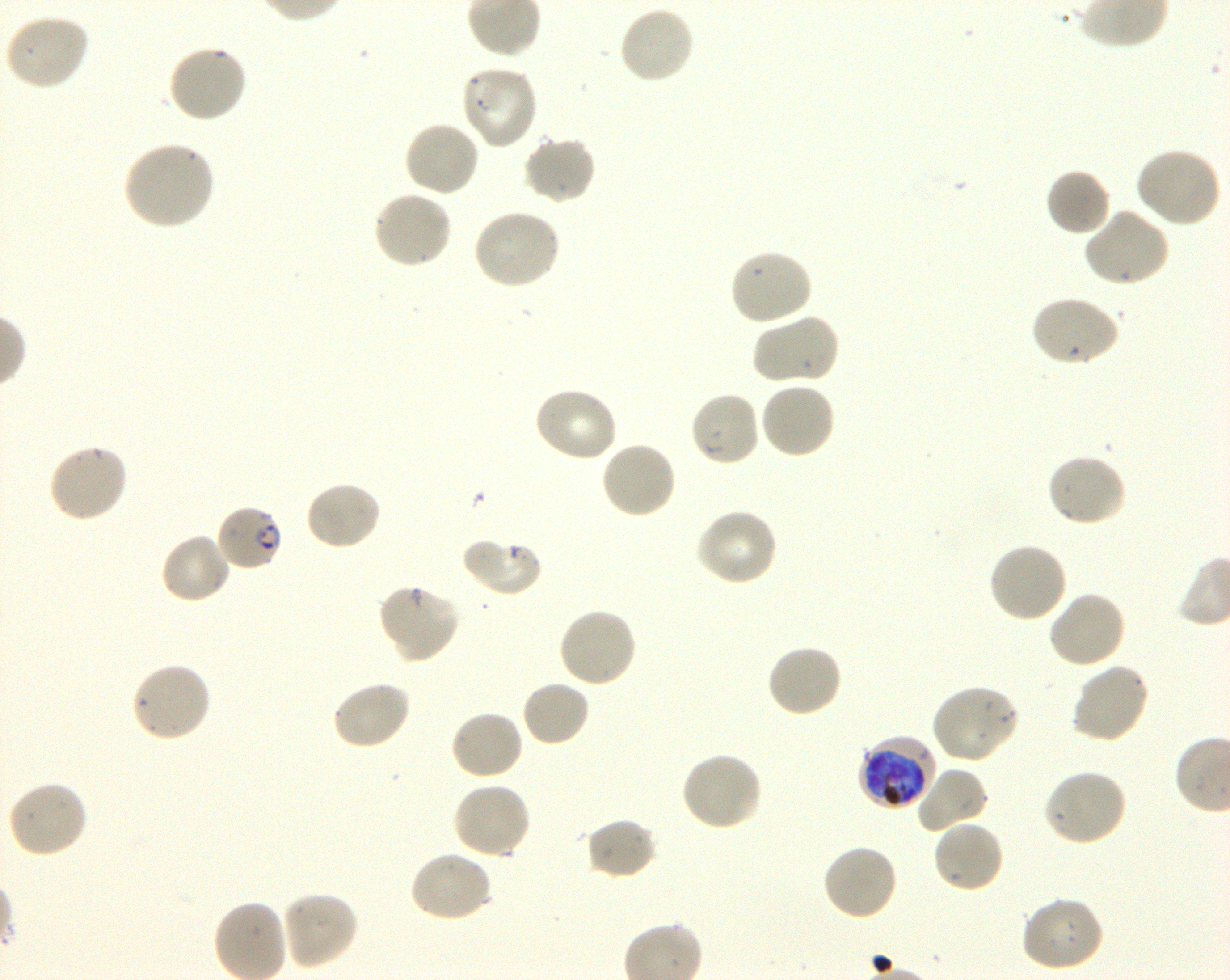
Not every red blood cell is marked. A life-cycle stage — or a range of stages, where the recorded stages span more than one — follows each staged infected red blood cell.
locations of uninfected red blood cells = approximate bounding boxes as [x1, y1, x2, y2] in pixels: [618, 4, 696, 84], [3, 13, 90, 91], [167, 42, 249, 123], [461, 64, 539, 150], [403, 120, 481, 199], [522, 135, 597, 206], [123, 141, 216, 231], [1134, 147, 1222, 229], [1045, 167, 1112, 237], [371, 190, 453, 270], [1082, 208, 1171, 288], [472, 209, 562, 290], [728, 248, 813, 327], [1029, 295, 1122, 368], [752, 313, 841, 386], [758, 380, 837, 460], [532, 386, 618, 464], [688, 390, 761, 468], [599, 440, 678, 520], [46, 443, 129, 524], [1046, 453, 1128, 528], [304, 479, 382, 551], [695, 507, 780, 587], [159, 532, 232, 606], [462, 537, 543, 598], [987, 541, 1068, 623], [377, 582, 460, 664], [1047, 591, 1126, 670], [558, 607, 638, 689], [766, 643, 844, 718], [130, 660, 212, 744], [1070, 661, 1151, 744], [330, 680, 412, 751], [520, 680, 590, 747], [931, 683, 1020, 765], [449, 709, 524, 781], [679, 751, 763, 832], [914, 766, 989, 833], [1042, 769, 1128, 847], [7, 778, 88, 859], [451, 779, 532, 860], [587, 815, 658, 881], [931, 819, 1005, 894], [820, 843, 899, 923], [408, 850, 493, 924], [279, 890, 358, 970], [1019, 896, 1105, 973]
objective = 100x, oil immersion, numerical aperture 1.30
field of view = single
preparation = thin blood smear
image size = 1230×980 pixels
locations of infected red blood cells = approximate bounding boxes as [x1, y1, x2, y2] in pixels: [215, 503, 284, 572] early ring to early trophozoite; [858, 735, 937, 812] early trophozoite to early schizont
donor blood group = O+
stain = Giemsa
culture = shaking in-vitro P. falciparum strain 3D7